Report the malaria status of this cell.
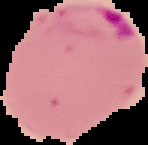

It is parasitized.

Summary:
  - Image type: segmented cell region with the area outside set to black
  - Preparation: thin blood smear
  - Image size: 148×145 pixels